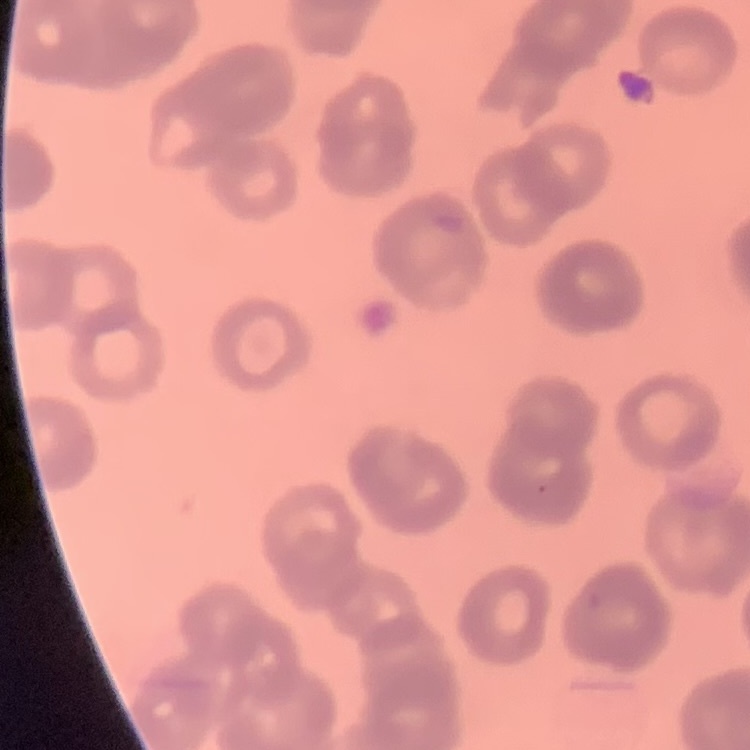
red blood cell morphology = rouleaux formation
image type = square crop of a larger photomicrograph
stain = Field's or Giemsa
preparation = thin peripheral smear